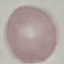

malaria status = uninfected
stain = Giemsa
image type = automatically extracted cell patch, resized to 64 × 64 pixels
capture = smartphone through the microscope eyepiece
preparation = thin smear